Name the parasite shown.
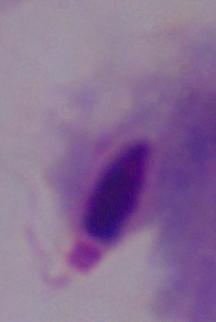

A trichomonad.

{
  "magnification": "1000x",
  "modality": "micrograph"
}